Give the extent of all Plasmodium malariae-infected red blood cells.
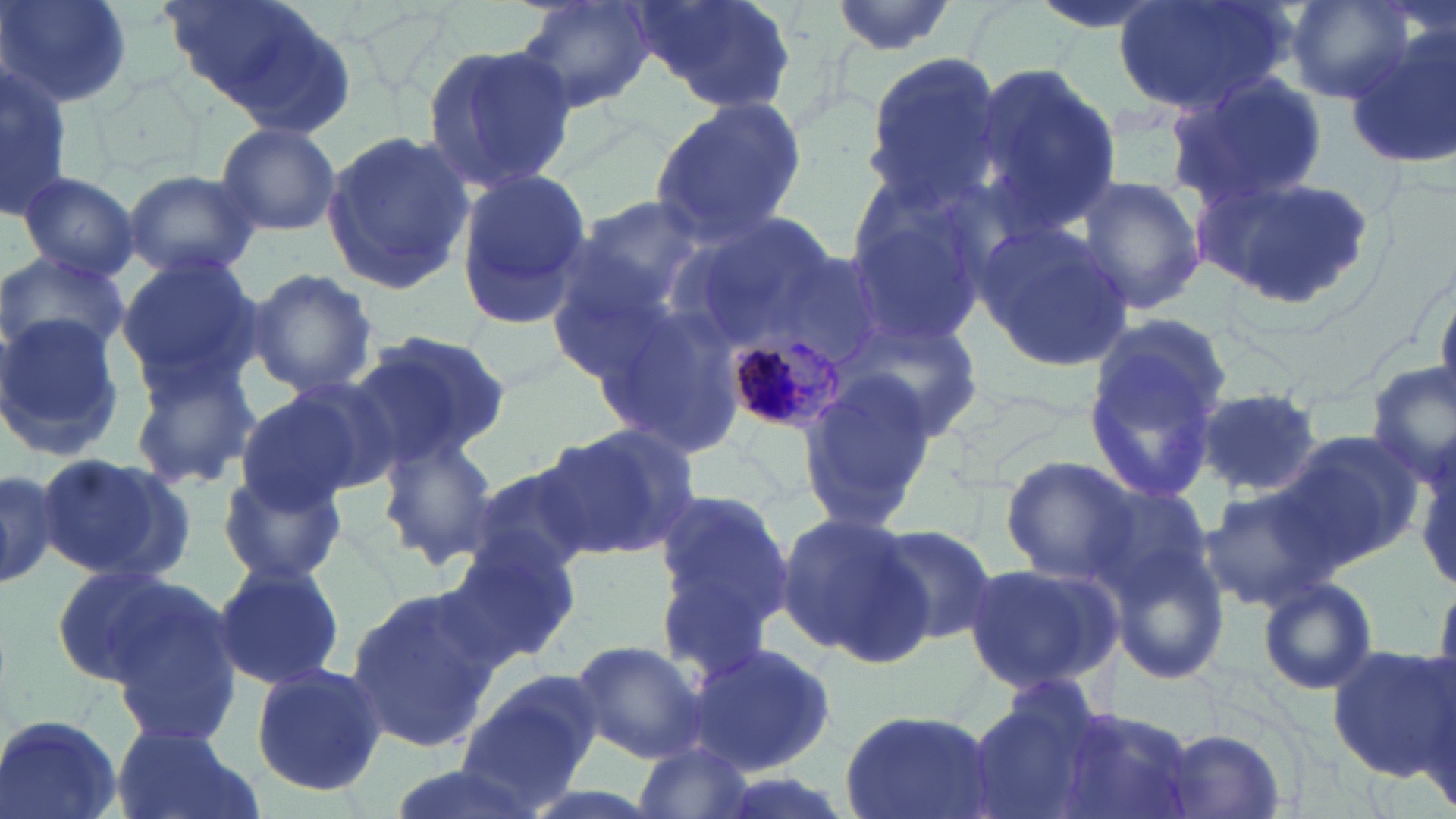
Approximate bounding boxes as (x1, y1, x2, y2) in pixels.
Plasmodium malariae-infected red blood cells: (727, 325, 851, 432).

Uninfected red blood cell locations: (2, 0, 134, 108), (161, 0, 347, 129), (511, 0, 659, 114), (630, 0, 798, 112), (826, 0, 958, 56), (1027, 0, 1172, 36), (1114, 0, 1288, 117), (1284, 0, 1416, 101), (1346, 36, 1455, 171), (421, 40, 576, 195), (861, 54, 1008, 207), (0, 62, 71, 218), (970, 63, 1125, 239), (1164, 73, 1328, 206), (650, 95, 807, 242), (214, 122, 342, 238), (321, 128, 475, 293), (120, 167, 259, 280), (1200, 168, 1385, 315), (16, 171, 142, 284), (453, 171, 592, 331), (1074, 174, 1208, 319), (547, 191, 762, 453), (841, 194, 992, 351), (971, 216, 1136, 377), (0, 250, 130, 367), (113, 256, 264, 398), (247, 269, 378, 395), (1434, 278, 1456, 411), (844, 310, 985, 446), (2, 312, 133, 460), (1083, 315, 1232, 500), (349, 330, 511, 467), (126, 356, 261, 491), (1363, 361, 1456, 489), (794, 369, 937, 531), (232, 385, 374, 513), (1195, 387, 1323, 498), (542, 421, 701, 563), (1278, 430, 1428, 567), (379, 433, 501, 566), (35, 453, 194, 583), (998, 455, 1144, 584), (0, 463, 59, 590), (461, 463, 596, 578), (216, 470, 346, 586), (1198, 482, 1338, 614), (650, 488, 796, 653), (775, 512, 927, 663), (867, 522, 998, 646), (1104, 526, 1235, 687), (434, 530, 583, 670), (964, 558, 1119, 693), (212, 561, 346, 689), (52, 564, 194, 686), (1258, 576, 1378, 695), (343, 585, 498, 754), (105, 597, 246, 748), (569, 640, 708, 762), (686, 641, 837, 775), (1326, 644, 1456, 778), (248, 662, 388, 797), (457, 672, 600, 812), (964, 684, 1119, 819), (836, 706, 1001, 819), (1048, 707, 1200, 819), (2, 711, 125, 818), (110, 728, 257, 819), (1162, 730, 1286, 818), (630, 744, 756, 819), (381, 763, 540, 819). Slide-level diagnosis: Plasmodium malariae. Image is 1456×819 pixels. 1000x magnification. May-Grünwald-Giemsa-stained preparation. Single field of view. Thin blood smear. Light microscopy.